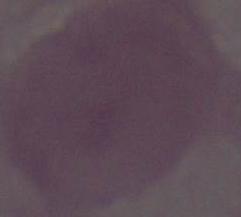 1000x magnification. Photomicrograph. An erythrocyte is seen.